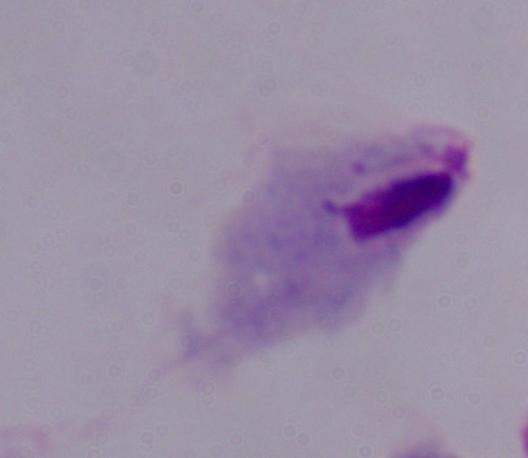 Micrograph. A trichomonad is seen. Captured at 1000x magnification.